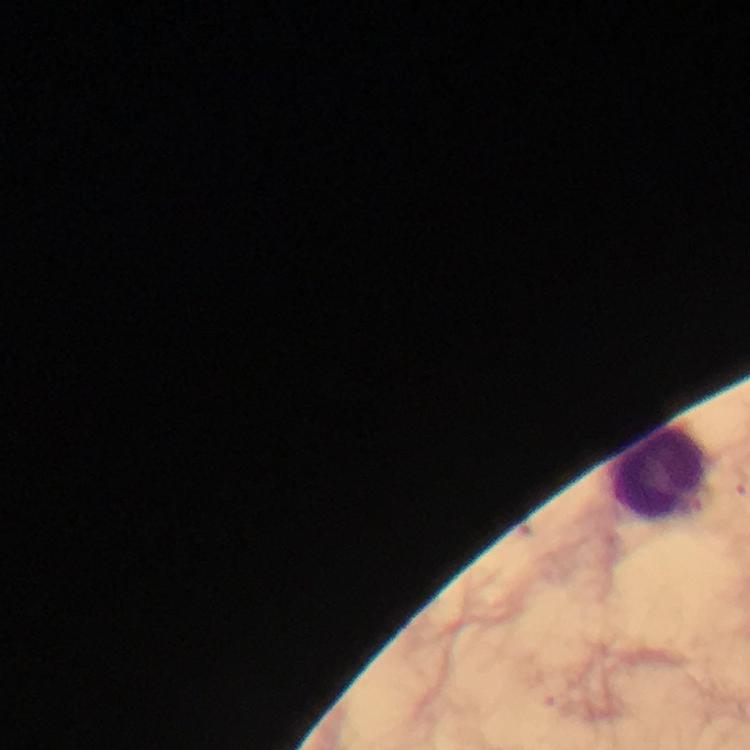

Approximate object centers, in pixels from the top-left corner.
Summary:
  - Leukocyte locations: (x=661, y=472)
  - Malaria parasites: none detected
  - Immersion oil: applied
  - Image size: 750×750 pixels
  - Magnification: 100x
  - Context: from a diagnostic examination for malaria
  - Cropped from: one field of view
  - Preparation: thick smear
  - Stain: Giemsa
  - Capture: smartphone mounted on the microscope